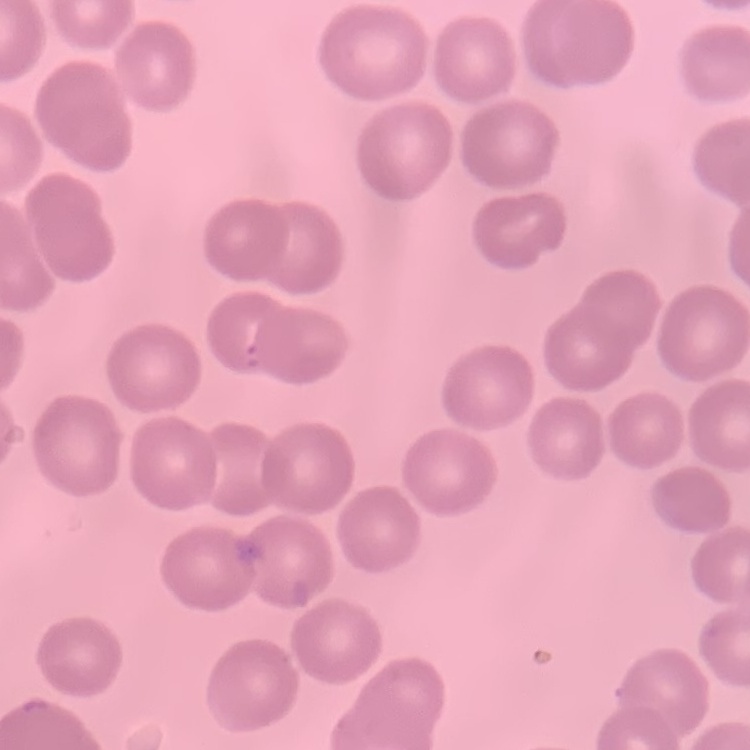

Summary:
  - Red blood cell morphology: no rouleaux formation
  - Image type: square crop of a larger photomicrograph
  - Preparation: thin blood film
  - Stain: Field's or Giemsa